State the blood parasite species.
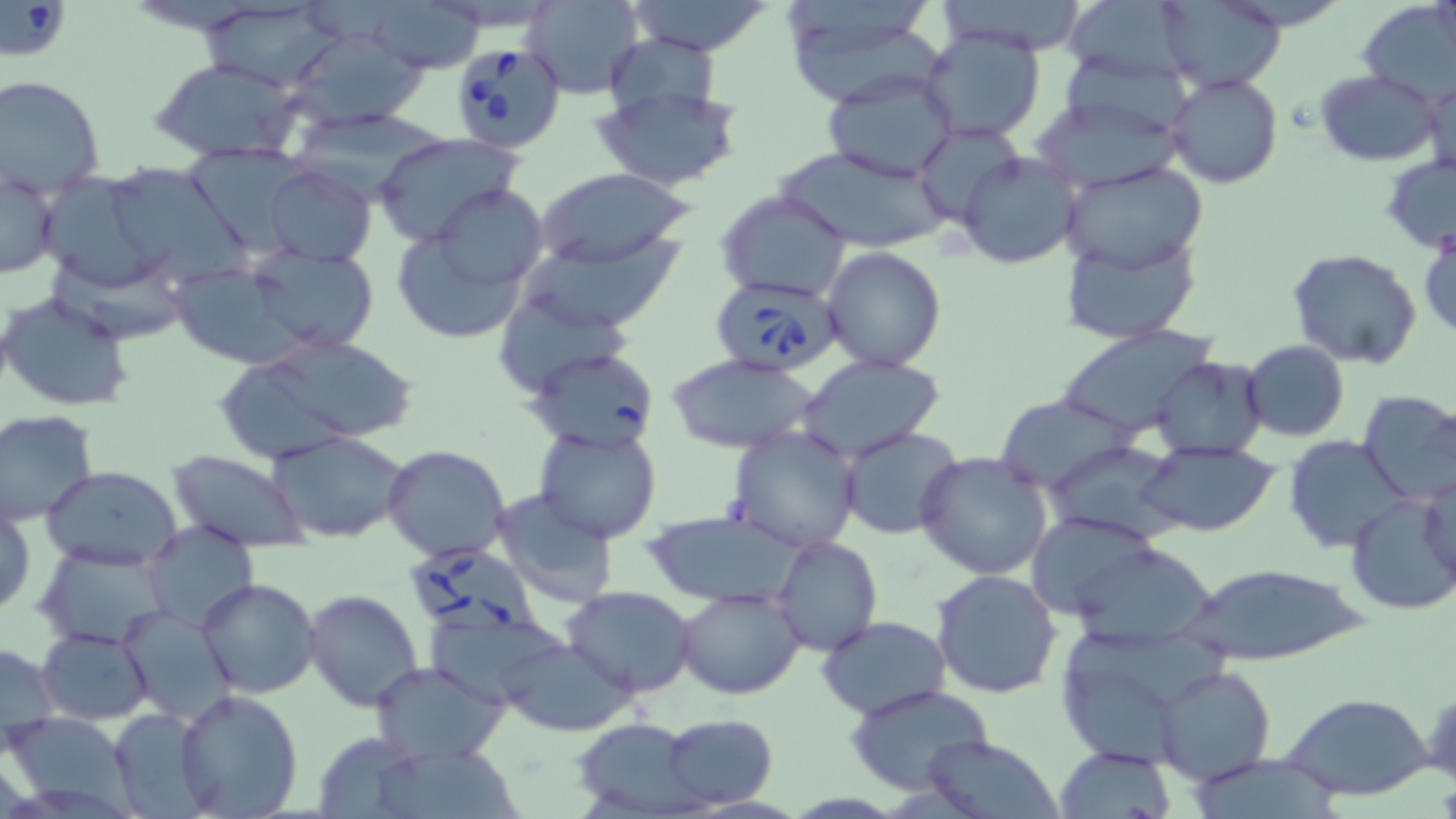
Babesia divergens.

Summary:
  - Coordinate format: approximate bounding boxes as [x1, y1, x2, y2] in pixels
  - Babesia divergens-infected red blood cell locations: [0, 2, 72, 61], [446, 38, 569, 155], [712, 277, 841, 377], [410, 547, 553, 643]
  - Uninfected red blood cell locations: [523, 0, 644, 99], [625, 0, 774, 56], [936, 0, 1090, 55], [1060, 1, 1199, 83], [1158, 1, 1286, 91], [202, 2, 344, 91], [371, 2, 485, 73], [1359, 3, 1454, 104], [781, 4, 939, 101], [283, 25, 429, 131], [921, 28, 1044, 144], [601, 37, 724, 125], [152, 58, 304, 163], [823, 67, 959, 183], [1316, 69, 1441, 166], [1167, 73, 1282, 188], [0, 74, 105, 193], [1423, 74, 1455, 179], [590, 82, 743, 190], [1029, 94, 1187, 193], [286, 109, 451, 192], [913, 124, 1026, 226], [371, 133, 522, 245], [183, 144, 305, 250], [775, 144, 948, 253], [957, 152, 1081, 269], [1381, 153, 1456, 253], [1061, 161, 1209, 273], [263, 164, 376, 266], [535, 166, 693, 272], [36, 167, 178, 292], [113, 169, 255, 284], [1, 172, 58, 280], [430, 181, 547, 294], [716, 190, 853, 303], [389, 210, 540, 345], [1419, 225, 1456, 339], [527, 230, 686, 331], [1059, 233, 1202, 345], [821, 246, 948, 372], [244, 247, 381, 355], [1286, 248, 1423, 369], [48, 253, 188, 348], [165, 260, 313, 372], [493, 287, 630, 399], [0, 292, 135, 414], [1056, 326, 1216, 439], [234, 333, 425, 450], [1242, 339, 1349, 442], [529, 346, 660, 455], [797, 351, 947, 462], [666, 353, 819, 454], [1151, 354, 1270, 459], [1355, 390, 1456, 505], [992, 395, 1140, 492], [0, 410, 100, 524], [727, 426, 861, 553], [840, 426, 965, 541], [535, 427, 662, 544], [267, 430, 410, 544], [1285, 438, 1410, 554], [1046, 439, 1183, 543], [1138, 440, 1281, 536], [382, 445, 512, 564], [167, 450, 311, 551], [914, 451, 1056, 581], [42, 464, 186, 569], [1418, 471, 1456, 598], [490, 489, 619, 608], [1344, 492, 1455, 616], [1, 496, 35, 624], [643, 510, 805, 607], [1023, 512, 1162, 619], [144, 526, 261, 632], [771, 537, 882, 657], [1068, 542, 1222, 648], [35, 545, 173, 650], [1177, 561, 1370, 666], [932, 569, 1063, 700], [196, 578, 321, 699], [564, 585, 698, 696], [677, 585, 805, 698], [303, 589, 425, 713], [117, 604, 238, 726], [817, 616, 952, 721], [36, 627, 154, 725], [501, 636, 632, 738], [0, 640, 58, 756], [369, 659, 512, 764], [1154, 665, 1275, 785], [844, 683, 997, 798], [175, 687, 304, 819], [1283, 691, 1433, 801], [112, 707, 213, 816], [2, 710, 136, 812], [662, 714, 778, 808], [569, 718, 703, 817], [316, 731, 425, 819], [918, 735, 1062, 819], [378, 741, 531, 819], [1054, 744, 1178, 818]
  - Image size: 1456×819 pixels
  - Modality: optical microscopy
  - Preparation: thin blood film
  - Field of view: one of a larger specimen
  - Magnification: 1000x
  - Stain: May-Grünwald-Giemsa